Comment on the morphology of the erythrocytes.
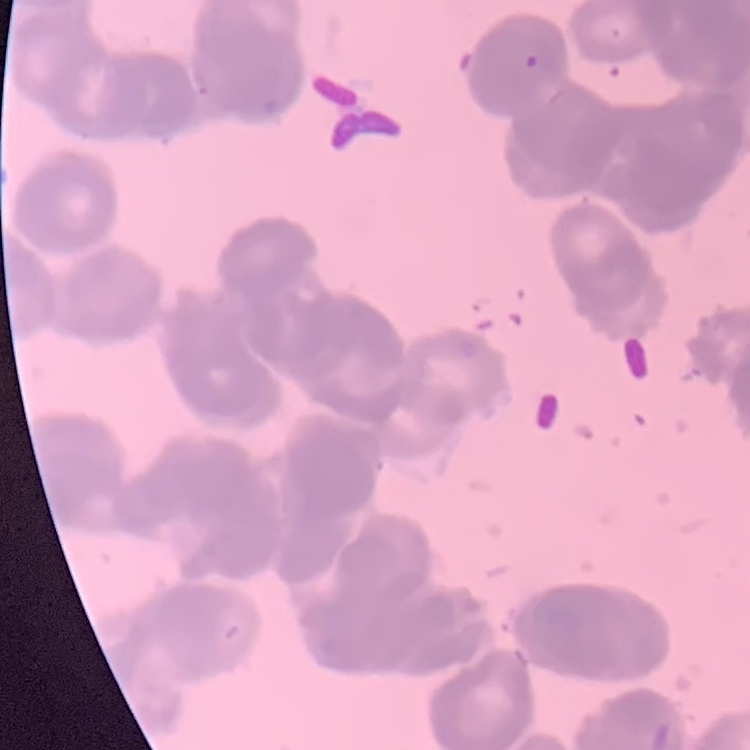
Rouleaux formation.

{
  "image_type": "one tile cut from a larger photomicrograph",
  "preparation": "thin blood smear",
  "stain": "Field's or Giemsa"
}